Classify this cell by malaria status.
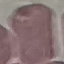
Uninfected.

Summary:
  - Preparation: thin smear
  - Stain: Giemsa
  - Image type: automatically extracted cell patch, resized to 64 × 64 pixels
  - Capture: smartphone through the microscope eyepiece